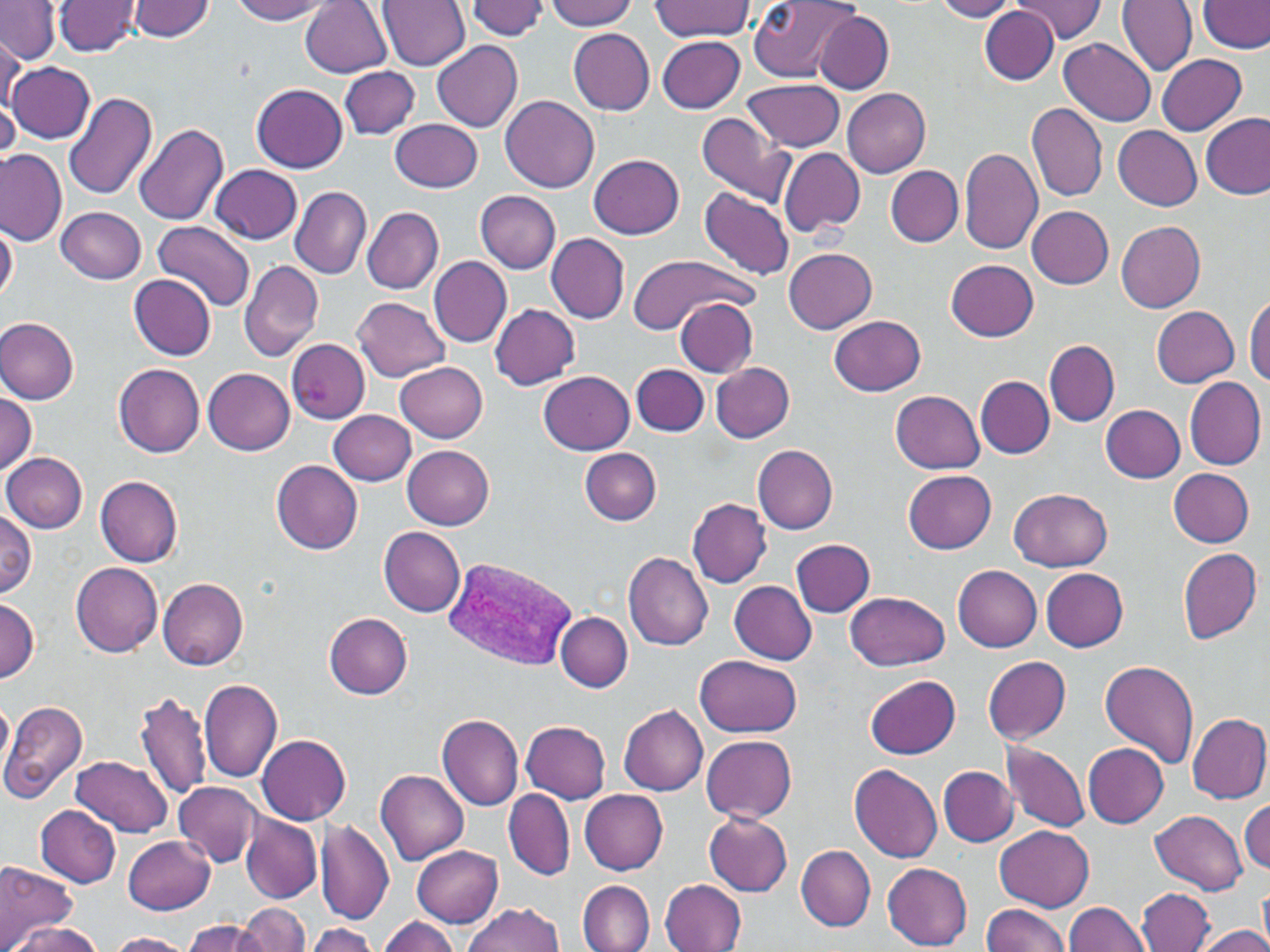 Approximate bounding boxes as (x1, y1, x2, y2) in pixels. Plasmodium vivax-infected red blood cell locations: (443, 555, 577, 670). Uninfected red blood cell locations: (53, 0, 143, 57), (129, 0, 215, 40), (231, 0, 334, 24), (375, 0, 468, 70), (543, 0, 638, 32), (747, 0, 860, 81), (931, 0, 1023, 21), (1011, 0, 1107, 42), (1117, 0, 1197, 78), (1199, 0, 1268, 53), (0, 1, 59, 63), (301, 1, 393, 78), (467, 1, 550, 39), (651, 1, 755, 40), (979, 7, 1058, 83), (815, 11, 894, 94), (568, 29, 655, 114), (657, 35, 746, 113), (1059, 38, 1155, 128), (0, 40, 23, 113), (432, 40, 524, 133), (1155, 53, 1247, 134), (8, 60, 96, 144), (339, 66, 421, 139), (745, 78, 845, 152), (251, 83, 349, 172), (841, 86, 931, 177), (63, 92, 158, 201), (501, 95, 599, 193), (1028, 101, 1108, 202), (1200, 111, 1269, 199), (696, 112, 795, 206), (391, 118, 483, 192), (134, 122, 229, 227), (1112, 125, 1203, 210), (958, 147, 1045, 254), (778, 148, 864, 239), (0, 151, 67, 246), (588, 154, 685, 240), (210, 164, 303, 244), (886, 166, 963, 246), (289, 185, 371, 280), (698, 186, 795, 281), (474, 189, 561, 273), (360, 204, 453, 382), (56, 206, 146, 285), (1027, 206, 1114, 289), (362, 207, 444, 294), (1116, 219, 1207, 312), (1, 221, 18, 303), (153, 221, 255, 311), (545, 233, 629, 323), (783, 248, 877, 334), (625, 252, 761, 336), (429, 257, 512, 348), (945, 258, 1041, 340), (238, 259, 324, 362), (128, 275, 217, 360), (1245, 293, 1270, 386), (351, 296, 450, 382), (676, 298, 758, 376), (489, 303, 580, 390), (1151, 305, 1240, 387), (830, 315, 926, 395), (1, 317, 79, 404), (286, 338, 371, 424), (1044, 341, 1120, 426), (395, 360, 489, 441), (711, 361, 795, 442), (112, 363, 206, 457), (632, 364, 709, 437), (203, 368, 295, 455), (539, 371, 634, 454), (976, 376, 1055, 458), (1185, 376, 1266, 470), (0, 390, 38, 476), (891, 390, 986, 474), (1100, 404, 1186, 483), (328, 410, 417, 486), (753, 444, 839, 533), (403, 445, 494, 529), (580, 447, 661, 525), (1, 452, 88, 533), (270, 459, 365, 555), (1168, 468, 1255, 546), (903, 469, 997, 553), (94, 474, 184, 566), (1009, 487, 1111, 572), (687, 499, 773, 588), (0, 509, 38, 598), (379, 527, 465, 617), (790, 538, 877, 618), (1176, 547, 1262, 644), (621, 552, 714, 651), (71, 561, 164, 656), (951, 565, 1041, 652), (1039, 568, 1128, 650), (157, 575, 249, 671), (730, 581, 816, 665), (846, 590, 951, 670), (0, 599, 40, 683), (325, 612, 413, 698), (556, 613, 633, 692), (696, 653, 803, 737), (982, 655, 1071, 743), (1098, 661, 1199, 771), (865, 674, 961, 760), (199, 678, 284, 783), (134, 690, 213, 800), (0, 695, 13, 788), (0, 700, 88, 804), (618, 705, 708, 797), (1185, 711, 1270, 804), (437, 713, 524, 811), (520, 720, 610, 803), (257, 734, 351, 825), (701, 735, 796, 822), (1000, 739, 1091, 833), (1081, 742, 1169, 827), (72, 755, 174, 836), (848, 764, 943, 864), (939, 766, 1019, 845), (376, 768, 468, 865), (175, 782, 260, 866), (503, 788, 573, 880), (580, 789, 669, 876), (1241, 800, 1270, 873), (35, 805, 121, 887), (1150, 809, 1248, 894), (239, 812, 323, 906), (703, 812, 794, 896), (315, 819, 394, 924), (995, 825, 1094, 912), (124, 835, 215, 914), (410, 844, 502, 925), (795, 844, 875, 932), (0, 858, 78, 948), (881, 863, 973, 949), (661, 878, 747, 952), (1258, 879, 1269, 948), (576, 880, 655, 952), (1137, 888, 1216, 952), (1064, 900, 1149, 952), (461, 902, 565, 952), (234, 904, 310, 952), (981, 904, 1071, 952), (377, 916, 463, 952), (185, 918, 269, 952), (10, 923, 103, 951), (301, 925, 381, 952), (1193, 925, 1270, 952), (105, 931, 192, 952). Slide-level diagnosis: Plasmodium vivax. Image is 1270×952 pixels. Light microscopy. 1000x magnification. May-Grünwald-Giemsa stain. Thin blood film. Single field of view.